Classify this cell by malaria status.
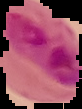

It is parasitized.

preparation = thin blood film
image type = segmented cell region on a black background
image size = 82×109 pixels